Give the position of every leukocyte.
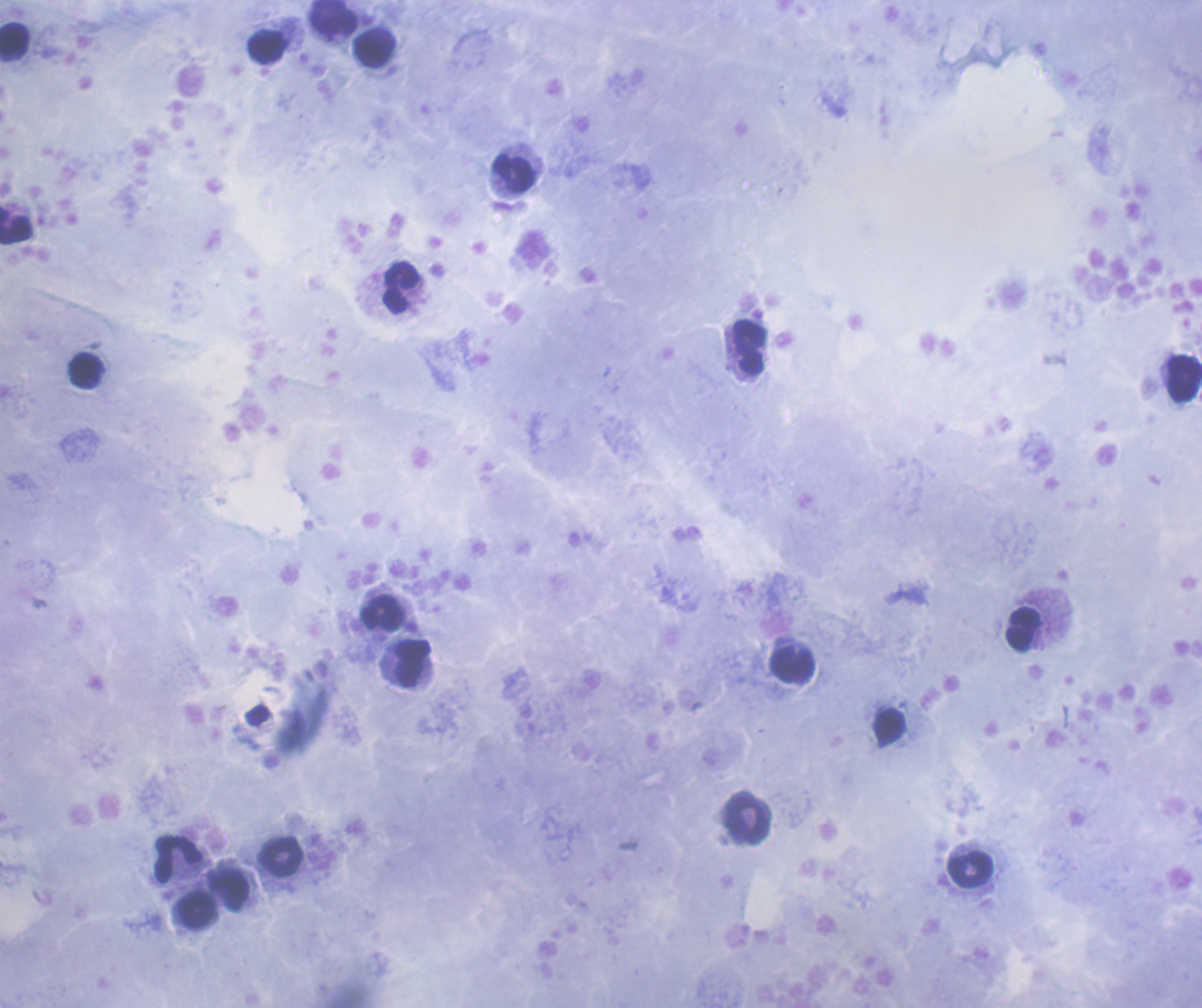

Approximate centers as [x, y] in pixels.
Leukocytes: [334, 18], [14, 42], [267, 46], [375, 47], [514, 172], [15, 225], [401, 286], [748, 347], [86, 371], [1184, 378], [383, 613], [1023, 628], [413, 663], [792, 665], [890, 727], [747, 819], [280, 856], [178, 858], [970, 870], [230, 890], [197, 910].

Summary:
  - Coloration quality: good
  - Magnification: 100x
  - Preparation: thick blood smear
  - Stain: Romanowsky
  - Background quality: satisfactory
  - Field of view: single
  - Context: previously used in an actual diagnosis
  - Result: no Plasmodium parasites seen
  - Image size: 1202×1008 pixels